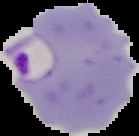
result = malaria parasites detected
image type = segmented cell region with the area outside set to black
image size = 139×136 pixels
preparation = thin blood smear